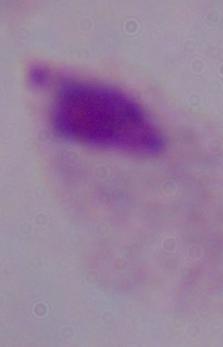
modality = micrograph
magnification = 1000x
identification = trichomonad